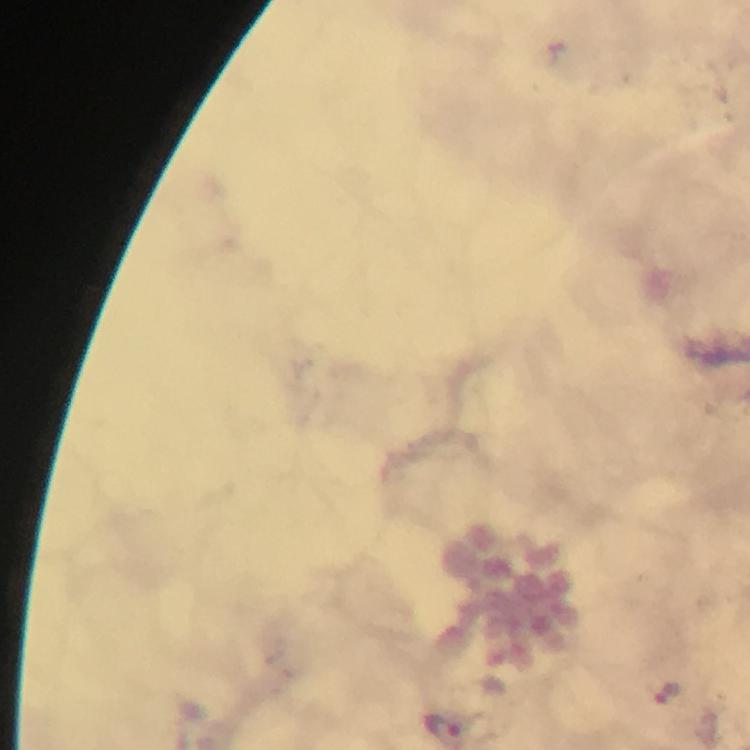

Approximate centers as {x, y} in pixels. Malaria parasite locations: {670, 692}, {442, 728}. Immersion oil applied. At 100x magnification. From a diagnostic examination for malaria. Giemsa-stained preparation. Thick smear. Smartphone photograph taken through a microscope. A crop from one field of view. Image is 750×750 pixels.